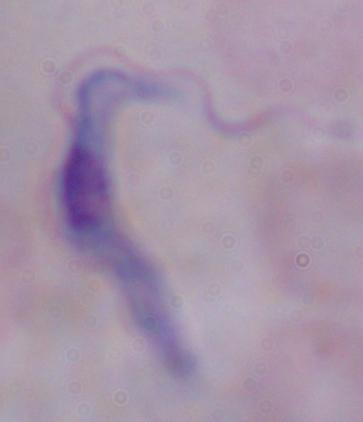

{
  "identification": "trypanosome",
  "modality": "photomicrograph",
  "magnification": "1000x"
}